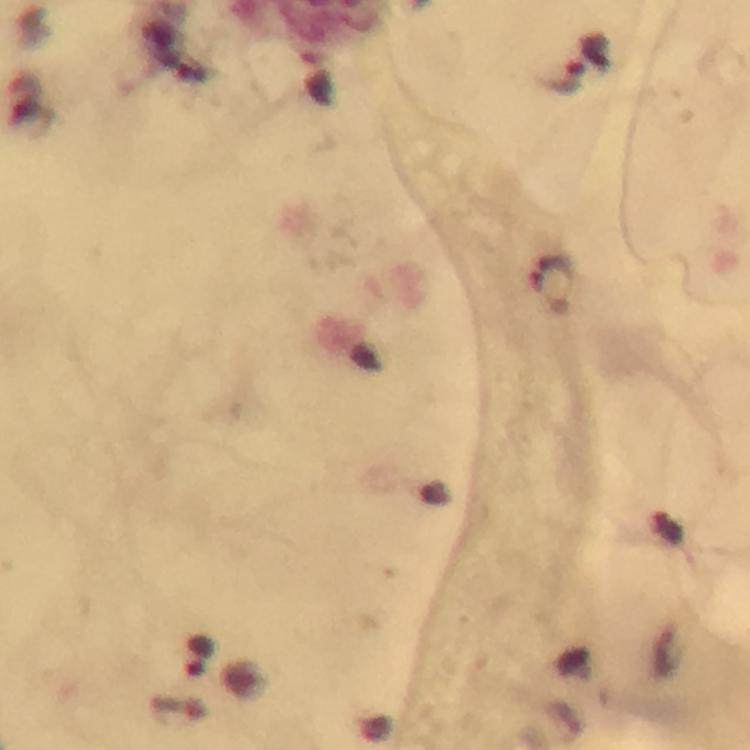

capture = smartphone photograph through a microscope
magnification = 100x
context = from a malaria diagnostic workup
preparation = thick smear
image size = 750×750 pixels
Plasmodium parasite locations = approximate centers as [x, y] in pixels: [552, 277], [197, 656]
immersion oil = applied
cropped from = a single field of view
stain = Giemsa